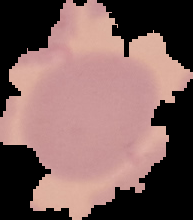

Summary:
  - Malaria status: uninfected
  - Preparation: thin blood film
  - Image size: 193×220 pixels
  - Image type: cell region segmented out of the field of view; surrounding area masked to black